Name the blood parasite species.
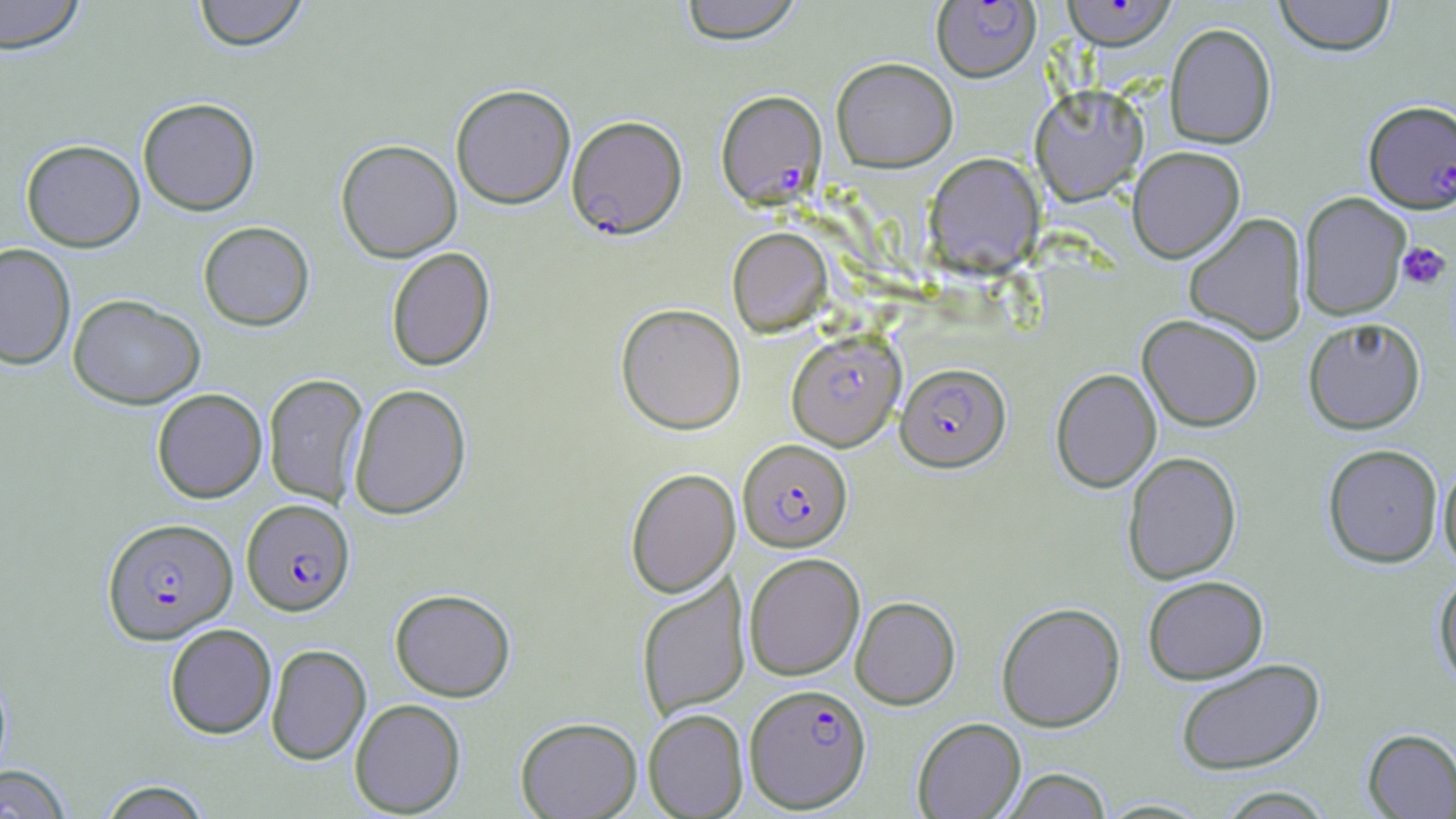
Plasmodium falciparum.

uninfected red blood cell locations = approximate bounding boxes as [x1, y1, x2, y2] in pixels: [0, 0, 87, 54], [192, 0, 309, 51], [679, 0, 804, 44], [1273, 0, 1397, 56], [1165, 22, 1277, 149], [831, 56, 958, 173], [1029, 83, 1148, 204], [451, 84, 576, 208], [137, 97, 261, 215], [21, 139, 145, 252], [335, 139, 462, 262], [1128, 146, 1245, 263], [924, 153, 1043, 275], [1298, 192, 1411, 320], [1183, 213, 1308, 344], [198, 221, 315, 331], [727, 227, 832, 337], [0, 242, 76, 370], [386, 247, 496, 371], [68, 294, 205, 409], [615, 303, 746, 434], [1138, 314, 1263, 431], [1303, 316, 1426, 434], [786, 330, 906, 451], [1050, 368, 1161, 492], [263, 373, 369, 508], [349, 383, 472, 520], [152, 388, 267, 503], [1322, 443, 1442, 567], [1122, 451, 1241, 584], [1438, 459, 1456, 575], [625, 467, 740, 599], [744, 552, 865, 680], [1433, 573, 1456, 691], [636, 574, 750, 721], [1142, 575, 1268, 683], [390, 588, 516, 702], [851, 596, 961, 709], [997, 601, 1126, 732], [165, 623, 277, 739], [266, 644, 371, 765], [1175, 658, 1326, 775], [349, 698, 466, 817], [643, 709, 749, 818], [515, 716, 642, 819], [912, 717, 1026, 818], [1362, 728, 1456, 818], [0, 764, 73, 818], [1001, 768, 1112, 818], [97, 779, 214, 819], [1216, 786, 1335, 818]
preparation = thin blood smear
magnification = 1000x
modality = optical microscopy
field of view = one of a larger specimen
image size = 1456×819 pixels
Plasmodium falciparum-infected red blood cell locations = approximate bounding boxes as [x1, y1, x2, y2] in pixels: [932, 1, 1040, 82], [1061, 1, 1178, 50], [715, 89, 827, 210], [1363, 100, 1456, 213], [567, 115, 688, 240], [896, 362, 1011, 472], [738, 439, 853, 552], [242, 498, 354, 616], [102, 517, 238, 644], [745, 683, 871, 812]
stain = May-Grünwald-Giemsa
platelet locations = approximate bounding boxes as [x1, y1, x2, y2] in pixels: [1396, 241, 1451, 291]